Locate every Plasmodium falciparum-infected red blood cell.
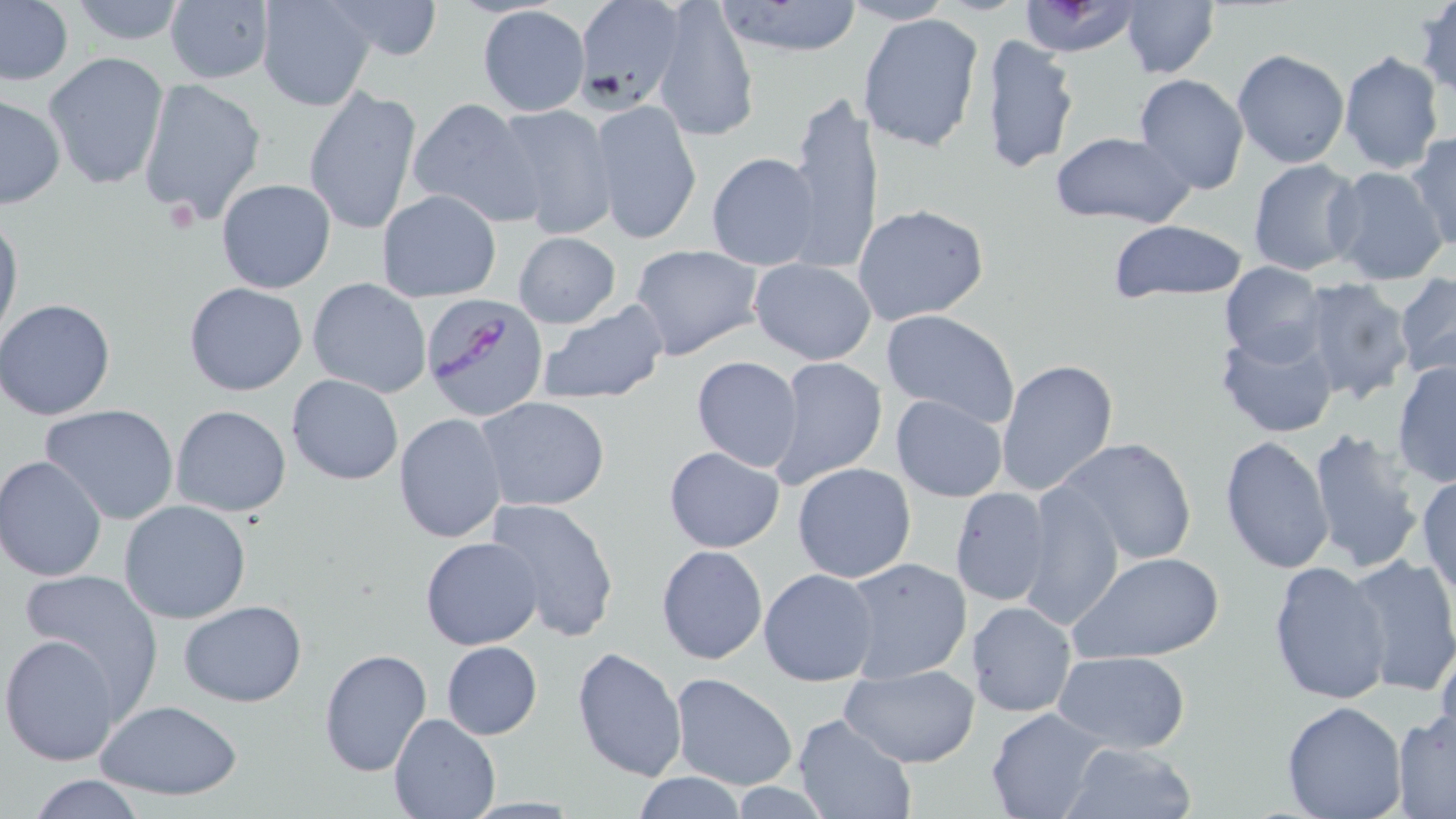

Approximate bounding boxes as named x1/y1/x2/y2 corners in pixels.
Plasmodium falciparum-infected red blood cells: (x1=423, y1=293, x2=548, y2=421).

Uninfected red blood cell locations: (x1=0, y1=0, x2=74, y2=87), (x1=63, y1=0, x2=193, y2=46), (x1=162, y1=0, x2=276, y2=85), (x1=255, y1=0, x2=376, y2=112), (x1=321, y1=0, x2=446, y2=61), (x1=572, y1=0, x2=685, y2=112), (x1=1120, y1=0, x2=1220, y2=79), (x1=1414, y1=0, x2=1456, y2=99), (x1=653, y1=1, x2=758, y2=141), (x1=712, y1=1, x2=866, y2=58), (x1=843, y1=1, x2=953, y2=25), (x1=1015, y1=1, x2=1142, y2=56), (x1=476, y1=4, x2=590, y2=117), (x1=857, y1=13, x2=986, y2=154), (x1=978, y1=34, x2=1082, y2=176), (x1=1337, y1=49, x2=1445, y2=174), (x1=1231, y1=50, x2=1349, y2=169), (x1=42, y1=53, x2=169, y2=191), (x1=1133, y1=73, x2=1250, y2=195), (x1=138, y1=78, x2=268, y2=224), (x1=303, y1=88, x2=422, y2=234), (x1=785, y1=91, x2=883, y2=271), (x1=0, y1=93, x2=67, y2=208), (x1=407, y1=97, x2=542, y2=226), (x1=589, y1=99, x2=702, y2=245), (x1=493, y1=103, x2=617, y2=240), (x1=1047, y1=131, x2=1195, y2=228), (x1=1407, y1=132, x2=1456, y2=255), (x1=706, y1=152, x2=821, y2=270), (x1=1247, y1=158, x2=1365, y2=276), (x1=1327, y1=166, x2=1451, y2=287), (x1=215, y1=179, x2=337, y2=294), (x1=377, y1=190, x2=501, y2=303), (x1=852, y1=203, x2=989, y2=325), (x1=0, y1=210, x2=23, y2=348), (x1=1104, y1=219, x2=1250, y2=302), (x1=512, y1=231, x2=621, y2=328), (x1=630, y1=245, x2=763, y2=358), (x1=749, y1=258, x2=876, y2=365), (x1=1220, y1=265, x2=1328, y2=364), (x1=1395, y1=274, x2=1456, y2=381), (x1=1296, y1=277, x2=1416, y2=405), (x1=306, y1=278, x2=433, y2=399), (x1=183, y1=281, x2=308, y2=396), (x1=0, y1=299, x2=119, y2=420), (x1=536, y1=302, x2=668, y2=406), (x1=881, y1=309, x2=1021, y2=429), (x1=1216, y1=325, x2=1339, y2=439), (x1=691, y1=356, x2=804, y2=471), (x1=769, y1=356, x2=887, y2=487), (x1=994, y1=357, x2=1120, y2=498), (x1=1391, y1=358, x2=1456, y2=487), (x1=286, y1=373, x2=405, y2=486), (x1=890, y1=393, x2=1007, y2=502), (x1=477, y1=396, x2=611, y2=513), (x1=40, y1=403, x2=181, y2=525), (x1=169, y1=405, x2=292, y2=516), (x1=393, y1=413, x2=508, y2=544), (x1=1303, y1=428, x2=1424, y2=570), (x1=1220, y1=435, x2=1335, y2=576), (x1=1055, y1=437, x2=1199, y2=567), (x1=664, y1=446, x2=785, y2=553), (x1=0, y1=456, x2=107, y2=581), (x1=793, y1=462, x2=917, y2=582), (x1=1415, y1=472, x2=1456, y2=596), (x1=1021, y1=482, x2=1124, y2=630), (x1=949, y1=487, x2=1054, y2=608), (x1=486, y1=497, x2=619, y2=640), (x1=118, y1=500, x2=253, y2=624), (x1=421, y1=537, x2=545, y2=651), (x1=656, y1=544, x2=768, y2=666), (x1=1071, y1=551, x2=1225, y2=665), (x1=1343, y1=553, x2=1456, y2=698), (x1=841, y1=557, x2=973, y2=683), (x1=1268, y1=560, x2=1392, y2=705), (x1=758, y1=568, x2=879, y2=686), (x1=18, y1=569, x2=160, y2=714), (x1=177, y1=600, x2=307, y2=707), (x1=968, y1=600, x2=1076, y2=718), (x1=1, y1=632, x2=125, y2=766), (x1=1434, y1=635, x2=1456, y2=757), (x1=441, y1=640, x2=543, y2=739), (x1=318, y1=646, x2=432, y2=777), (x1=571, y1=646, x2=688, y2=781), (x1=1051, y1=652, x2=1192, y2=751), (x1=839, y1=665, x2=980, y2=768), (x1=668, y1=672, x2=799, y2=790), (x1=97, y1=700, x2=243, y2=800), (x1=1280, y1=700, x2=1409, y2=819), (x1=986, y1=706, x2=1111, y2=819), (x1=1391, y1=710, x2=1456, y2=816), (x1=388, y1=711, x2=500, y2=818), (x1=793, y1=714, x2=915, y2=818), (x1=1059, y1=740, x2=1200, y2=819), (x1=631, y1=771, x2=747, y2=818), (x1=24, y1=775, x2=151, y2=818). Slide-level diagnosis: Plasmodium falciparum. 1000x magnification. Image is 1456×819 pixels. One field of a larger specimen. Thin blood film. Optical microscopy. May-Grünwald-Giemsa-stained preparation.